Identify the blood parasite species.
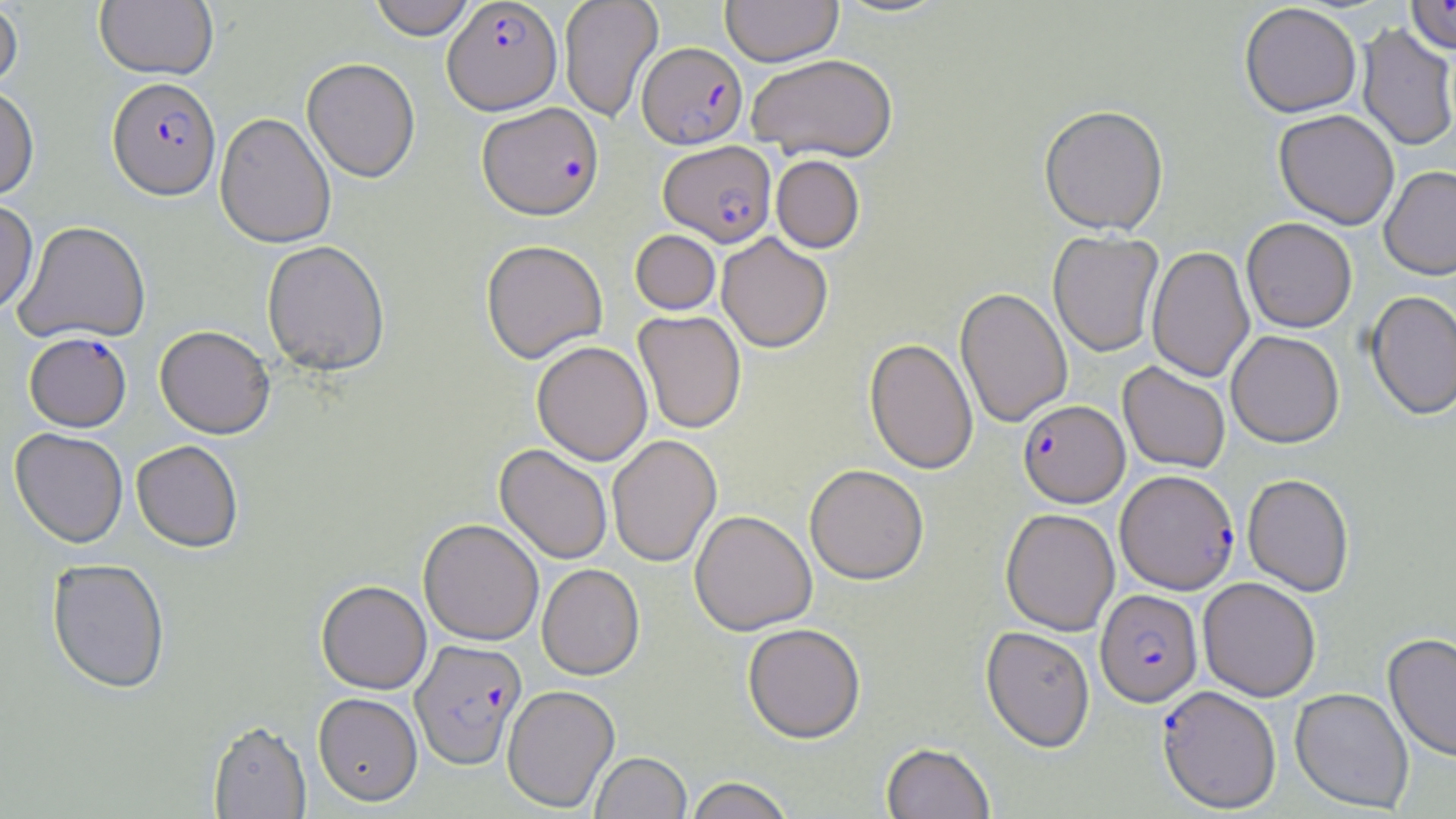

Plasmodium falciparum.

Approximate bounding boxes as named x1/y1/x2/y2 corners in pixels. Plasmodium falciparum-infected red blood cell locations: (x1=1407, y1=0, x2=1456, y2=55), (x1=442, y1=1, x2=562, y2=116), (x1=638, y1=43, x2=748, y2=150), (x1=106, y1=79, x2=222, y2=204), (x1=477, y1=105, x2=604, y2=223), (x1=659, y1=141, x2=777, y2=248), (x1=25, y1=334, x2=131, y2=434), (x1=1018, y1=400, x2=1129, y2=507), (x1=1115, y1=469, x2=1239, y2=595), (x1=1095, y1=589, x2=1203, y2=707), (x1=410, y1=640, x2=527, y2=770), (x1=1157, y1=686, x2=1282, y2=813). Uninfected red blood cell locations: (x1=94, y1=0, x2=218, y2=83), (x1=368, y1=0, x2=476, y2=42), (x1=559, y1=0, x2=663, y2=122), (x1=720, y1=0, x2=843, y2=67), (x1=0, y1=2, x2=22, y2=99), (x1=1239, y1=3, x2=1362, y2=119), (x1=1357, y1=23, x2=1456, y2=152), (x1=746, y1=54, x2=898, y2=163), (x1=301, y1=59, x2=420, y2=186), (x1=0, y1=86, x2=39, y2=203), (x1=1038, y1=106, x2=1169, y2=238), (x1=1274, y1=111, x2=1399, y2=229), (x1=215, y1=115, x2=336, y2=250), (x1=771, y1=155, x2=865, y2=253), (x1=1380, y1=167, x2=1456, y2=281), (x1=0, y1=201, x2=38, y2=317), (x1=1242, y1=219, x2=1357, y2=333), (x1=14, y1=222, x2=151, y2=346), (x1=630, y1=230, x2=721, y2=316), (x1=1048, y1=231, x2=1163, y2=357), (x1=717, y1=233, x2=832, y2=353), (x1=261, y1=242, x2=391, y2=378), (x1=481, y1=242, x2=607, y2=365), (x1=1146, y1=246, x2=1255, y2=383), (x1=955, y1=288, x2=1072, y2=428), (x1=1365, y1=291, x2=1456, y2=421), (x1=633, y1=311, x2=747, y2=434), (x1=154, y1=328, x2=275, y2=441), (x1=1226, y1=330, x2=1344, y2=448), (x1=864, y1=338, x2=978, y2=475), (x1=532, y1=342, x2=653, y2=466), (x1=1118, y1=362, x2=1230, y2=474), (x1=9, y1=429, x2=128, y2=551), (x1=607, y1=435, x2=722, y2=568), (x1=131, y1=443, x2=243, y2=555), (x1=494, y1=445, x2=612, y2=565), (x1=804, y1=464, x2=929, y2=586), (x1=1242, y1=473, x2=1354, y2=597), (x1=1001, y1=508, x2=1120, y2=635), (x1=689, y1=510, x2=817, y2=636), (x1=418, y1=520, x2=544, y2=646), (x1=46, y1=561, x2=170, y2=696), (x1=537, y1=564, x2=645, y2=681), (x1=1198, y1=577, x2=1321, y2=702), (x1=316, y1=582, x2=431, y2=696), (x1=742, y1=624, x2=866, y2=743), (x1=981, y1=626, x2=1095, y2=752), (x1=1383, y1=633, x2=1456, y2=763), (x1=502, y1=685, x2=620, y2=812), (x1=1290, y1=688, x2=1414, y2=813), (x1=313, y1=693, x2=423, y2=807), (x1=208, y1=721, x2=311, y2=819), (x1=881, y1=743, x2=995, y2=819), (x1=590, y1=752, x2=691, y2=819), (x1=684, y1=776, x2=795, y2=819). Single field of view. Optical microscopy. Captured at 1000x magnification. Thin blood film. May-Grünwald-Giemsa stain. Image is 1456×819 pixels.